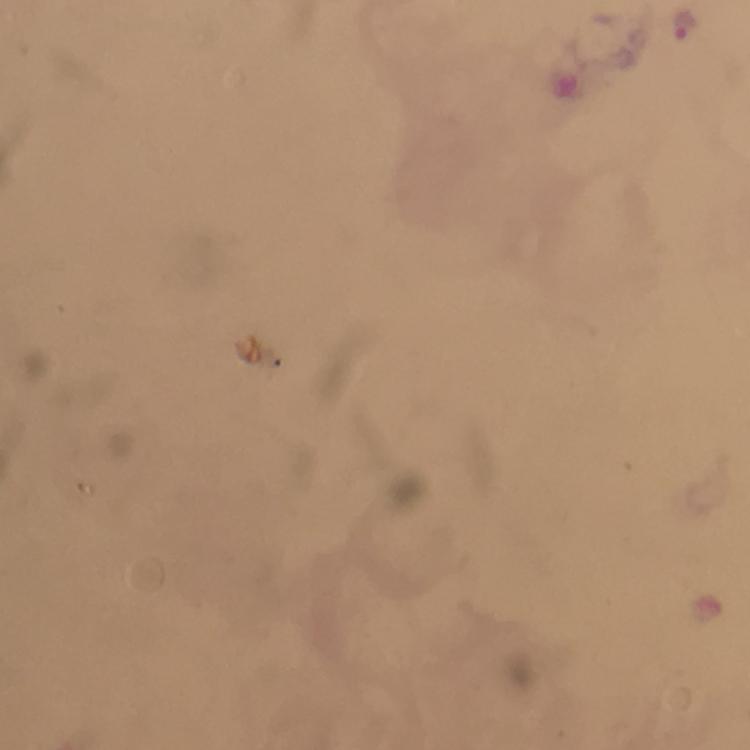
malaria parasite locations = approximate centers as [x, y] in pixels: [683, 25]
immersion oil = used
preparation = thick blood film
image size = 750×750 pixels
magnification = 100x
cropped from = a single field of view
stain = Giemsa
capture = smartphone photograph through a microscope
context = from a malaria diagnostic workup